State which parasite is depicted.
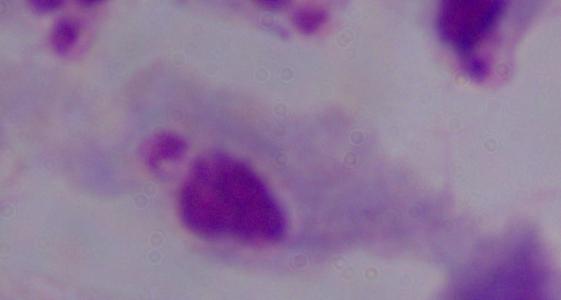
A trichomonad.

modality = micrograph
magnification = 1000x